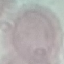

{
  "result": "no malaria parasites seen",
  "preparation": "thin blood film",
  "image_type": "cell patch, automatically extracted from a larger field of view and resized to 64 × 64 pixels",
  "stain": "Giemsa",
  "capture": "smartphone camera at the microscope eyepiece"
}